State which parasite is depicted.
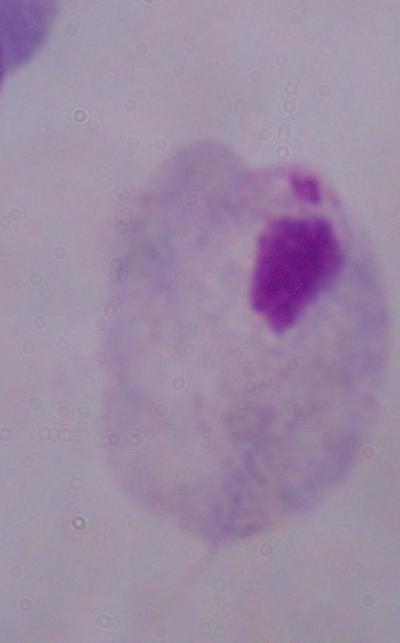
A trichomonad.

Summary:
  - Magnification: 1000x
  - Modality: micrograph